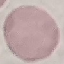
Summary:
  - Malaria status: uninfected
  - Preparation: thin blood smear
  - Image type: automatically extracted cell patch, resized to 64 × 64 pixels
  - Stain: Giemsa
  - Capture: smartphone through the microscope eyepiece